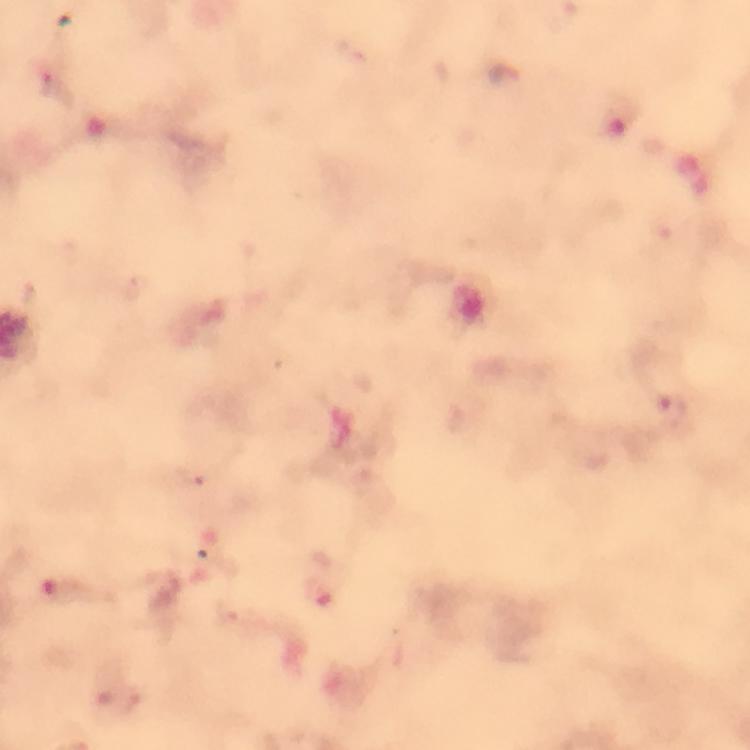
Approximate centers as {x, y} in pixels. Plasmodium parasite locations: {354, 51}, {47, 83}, {671, 409}, {193, 473}. At 100x magnification. A crop from one field of view. Giemsa-stained preparation. Image is 750×750 pixels. Thick smear. From a malaria diagnostic workup. Photographed with a smartphone mounted on the microscope. Immersion oil was used.